Assess this cell for malaria.
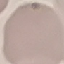

It is uninfected.

image type = cell patch, automatically extracted from a larger field of view and resized to 64 × 64 pixels
stain = Giemsa
capture = smartphone camera at the microscope eyepiece
preparation = thin blood film